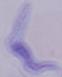
identification: trypanosome
magnification: 1000x
modality: photomicrograph